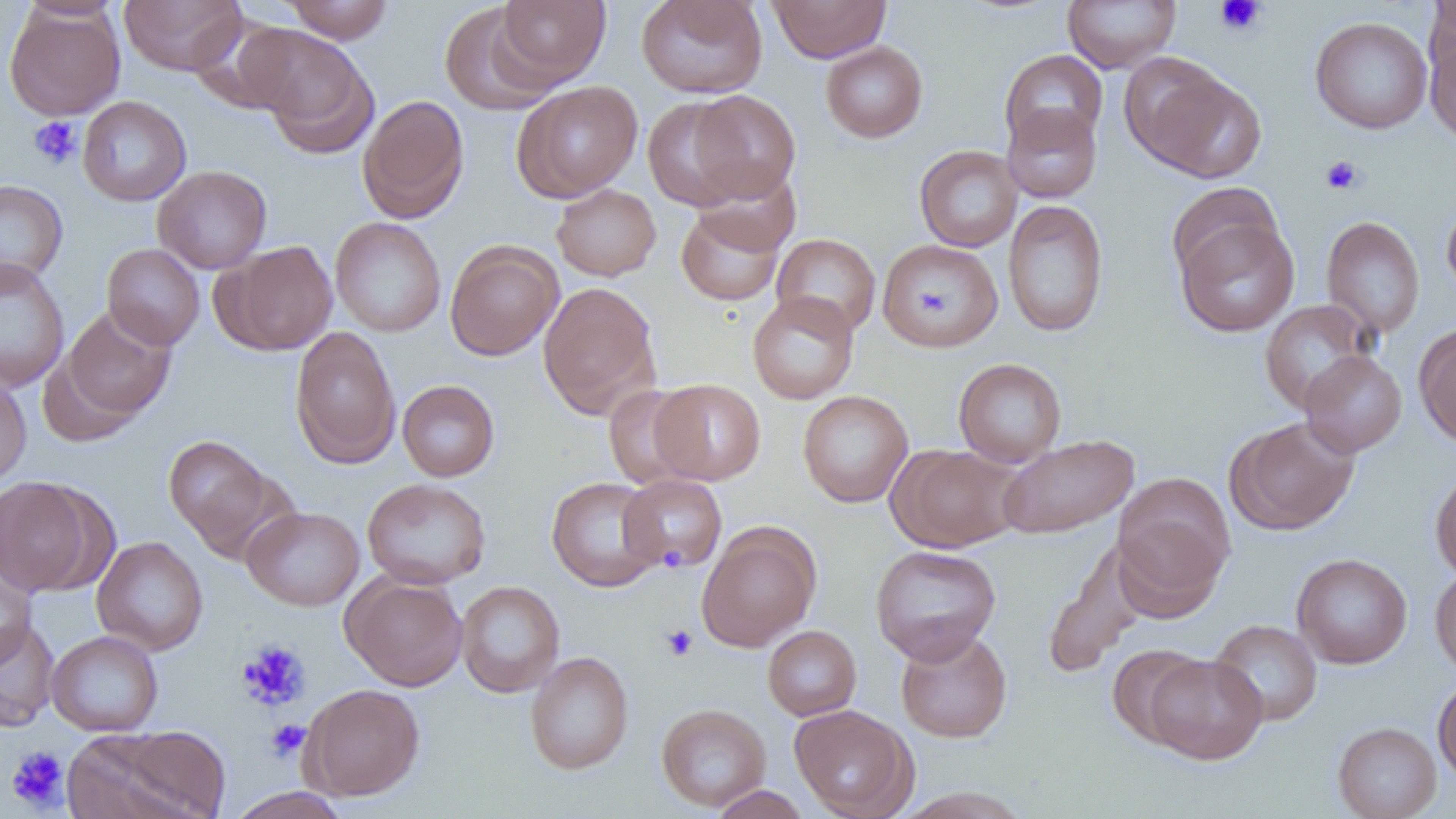
{
  "slide_level_diagnosis": "no evidence of blood parasites",
  "preparation": "thin blood film",
  "field_of_view": "one of a larger specimen",
  "magnification": "1000x",
  "modality": "optical microscopy",
  "platelet_locations": "approximate bounding boxes as (x1,y1)-(x2,y2) corner pairs in pixels: (1213,0)-(1266,37), (28,116)-(82,170), (1321,155)-(1365,196), (665,546)-(685,564), (660,624)-(698,662), (236,639)-(311,712), (265,719)-(310,761), (5,745)-(70,812)",
  "image_size": "1456×819 pixels",
  "uninfected_red_blood_cell_locations": "approximate bounding boxes as (x1,y1)-(x2,y2) corner pairs in pixels: (16,0)-(125,21), (119,0)-(246,75), (282,0)-(395,43), (494,0)-(610,87), (636,0)-(768,99), (768,0)-(891,63), (1425,0)-(1455,78), (1063,1)-(1180,73), (439,3)-(560,116), (4,4)-(125,120), (1310,16)-(1433,134), (1425,25)-(1456,147), (242,26)-(379,157), (820,40)-(928,143), (999,49)-(1107,151), (1128,62)-(1266,182), (512,80)-(643,201), (687,90)-(801,203), (357,94)-(470,223), (77,96)-(191,207), (642,96)-(751,212), (1002,104)-(1102,203), (914,145)-(1023,252), (153,165)-(272,274), (693,166)-(802,257), (0,179)-(68,287), (1166,181)-(1282,285), (551,183)-(661,281), (1440,199)-(1456,301), (1002,200)-(1110,338), (675,204)-(786,306), (1174,216)-(1300,338), (1321,216)-(1425,338), (330,217)-(446,337), (771,233)-(881,338), (878,238)-(1003,351), (219,240)-(337,355), (444,240)-(563,361), (101,243)-(205,350), (0,258)-(70,392), (538,282)-(661,418), (747,291)-(859,404), (1259,300)-(1377,413), (60,306)-(177,424), (1415,324)-(1456,449), (289,326)-(401,468), (1299,351)-(1407,457), (953,358)-(1067,467), (0,373)-(31,487), (649,378)-(766,485), (397,380)-(500,482), (603,383)-(701,490), (797,389)-(913,508), (1226,416)-(1360,535), (997,433)-(1139,538), (163,434)-(279,555), (888,444)-(1023,553), (1430,466)-(1456,580), (617,473)-(728,573), (1112,474)-(1234,612), (0,476)-(101,595), (362,477)-(491,589), (546,477)-(663,592), (242,506)-(365,611), (696,523)-(820,652), (92,536)-(208,655), (870,544)-(1001,664), (1041,544)-(1147,677), (1290,552)-(1413,669), (1430,565)-(1456,679), (0,567)-(36,670), (341,573)-(468,690), (456,581)-(565,698), (0,617)-(60,732), (1209,619)-(1323,726), (762,625)-(862,721), (896,628)-(1012,743), (46,630)-(163,736), (1106,644)-(1209,747), (525,651)-(634,774), (1144,654)-(1268,764), (1432,676)-(1456,788), (301,683)-(425,801), (656,703)-(771,811), (789,704)-(917,818), (1332,721)-(1442,819), (93,724)-(232,819), (708,784)-(811,818), (227,787)-(352,819)"
}